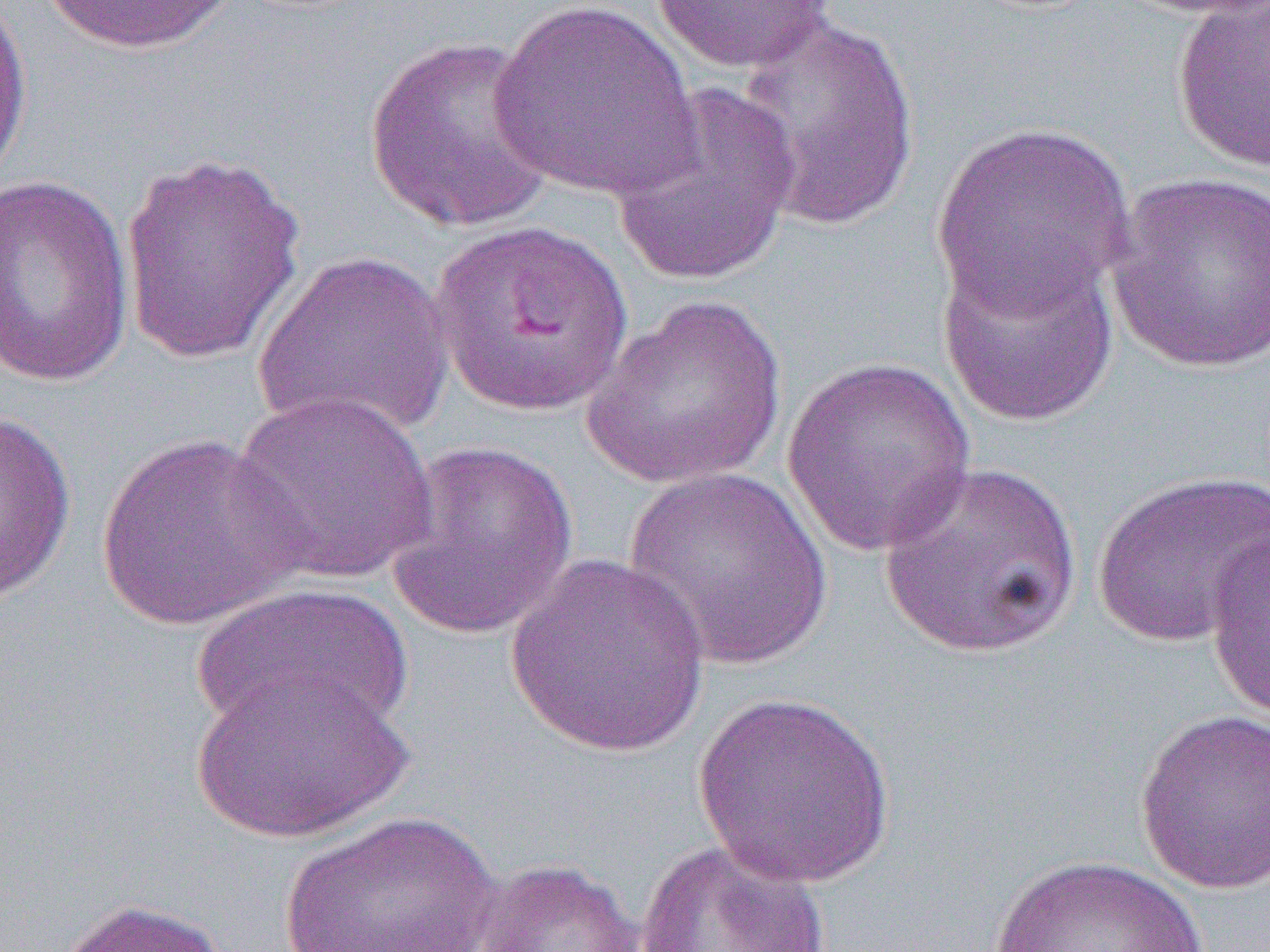
Approximate bounding boxes as (x1, y1, x2, y2) in pixels. Uninfected red blood cell locations: (38, 0, 238, 56), (1119, 0, 1270, 18), (0, 1, 34, 194), (488, 1, 703, 202), (649, 1, 836, 73), (1171, 2, 1270, 175), (728, 14, 923, 235), (363, 35, 558, 235), (610, 82, 802, 288), (930, 121, 1136, 318), (118, 149, 308, 368), (1105, 170, 1270, 375), (0, 173, 137, 388), (429, 218, 635, 420), (936, 244, 1120, 427), (251, 249, 456, 441), (582, 294, 789, 491), (780, 356, 977, 557), (230, 390, 440, 585), (0, 407, 78, 610), (93, 433, 311, 632), (383, 439, 579, 641), (878, 460, 1081, 660), (624, 466, 833, 671), (1091, 468, 1270, 648), (1204, 530, 1270, 728), (504, 553, 714, 758), (189, 583, 414, 741), (190, 668, 415, 844), (690, 690, 898, 889), (1134, 709, 1269, 895), (277, 808, 504, 952), (635, 839, 834, 952), (985, 853, 1219, 952), (472, 858, 645, 952), (48, 896, 233, 952). Slide-level diagnosis: Plasmodium falciparum. Optical microscopy. One field of a larger specimen. Thin blood film. Image is 1270×952 pixels. 1000x magnification.